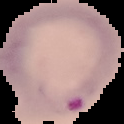
Summary:
  - Preparation: thin blood smear
  - Result: malaria parasites identified
  - Image type: cell region segmented out of the field of view; surrounding area masked to black
  - Image size: 124×124 pixels